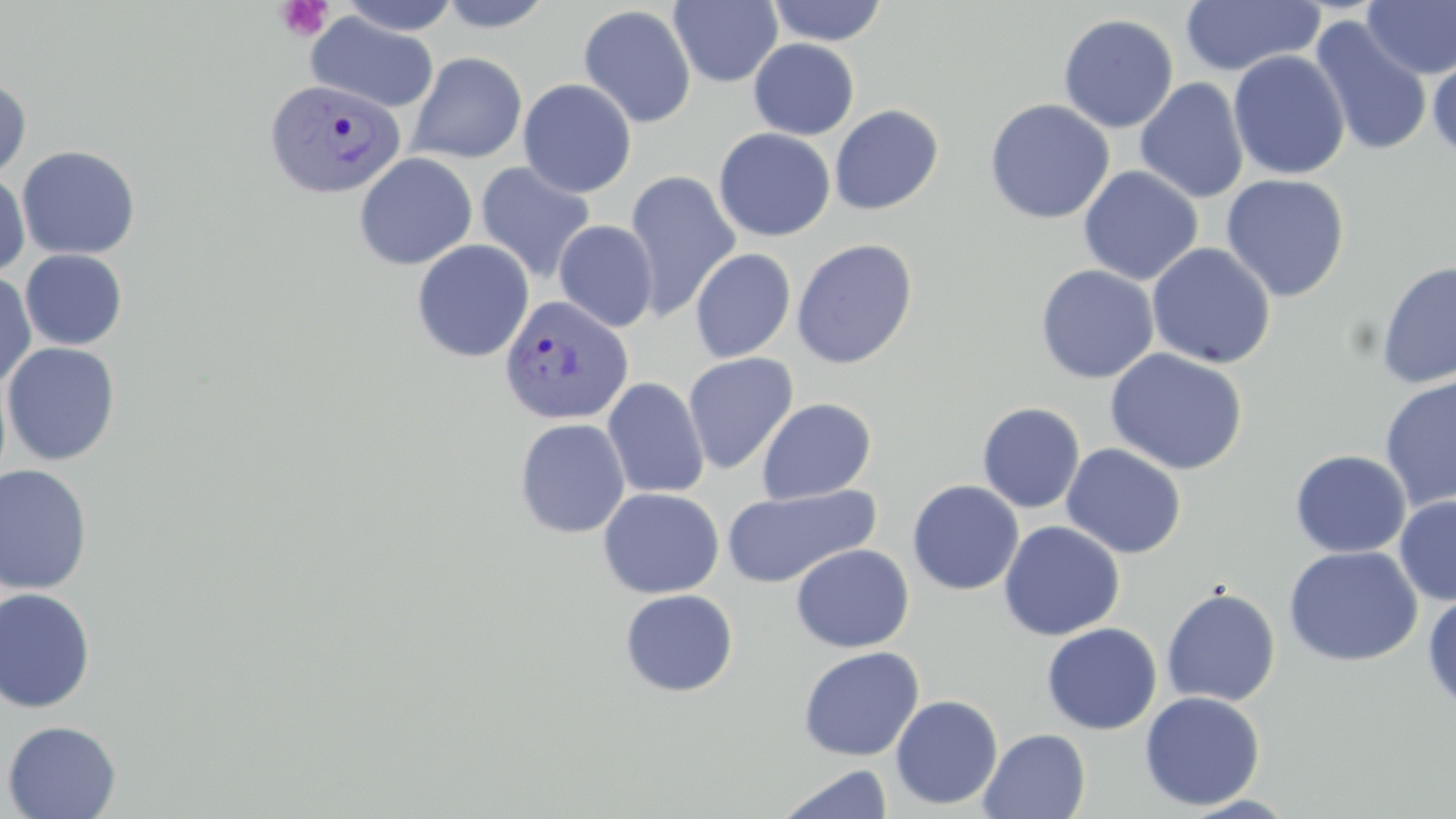

{
  "slide_level_diagnosis": "Plasmodium vivax",
  "image_size": "1456×819 pixels",
  "field_of_view": "single",
  "stain": "May-Grünwald-Giemsa",
  "plasmodium_vivax_infected_red_blood_cell_locations": "approximate bounding boxes as (x1, y1, x2, y2) in pixels: (263, 77, 406, 202), (499, 295, 634, 426)",
  "uninfected_red_blood_cell_locations": "approximate bounding boxes as (x1, y1, x2, y2) in pixels: (437, 0, 555, 32), (668, 0, 783, 87), (1179, 0, 1324, 77), (338, 1, 460, 35), (766, 1, 888, 46), (1361, 1, 1456, 79), (578, 5, 696, 128), (306, 13, 438, 113), (1057, 13, 1179, 133), (1308, 15, 1433, 157), (748, 39, 860, 140), (1428, 47, 1456, 163), (1228, 50, 1350, 181), (407, 52, 527, 164), (0, 77, 31, 182), (1135, 77, 1249, 204), (517, 78, 637, 198), (984, 98, 1115, 224), (829, 104, 944, 215), (713, 128, 836, 242), (17, 145, 141, 260), (354, 152, 478, 271), (475, 161, 597, 284), (1078, 165, 1203, 286), (624, 170, 741, 321), (0, 171, 30, 278), (1220, 173, 1350, 302), (554, 220, 658, 333), (791, 238, 918, 369), (411, 240, 535, 362), (1147, 242, 1276, 369), (19, 249, 128, 350), (690, 249, 796, 363), (1375, 259, 1456, 390), (1035, 264, 1159, 384), (0, 272, 37, 388), (1, 342, 121, 466), (1105, 348, 1248, 475), (682, 353, 799, 474), (1378, 373, 1456, 511), (602, 378, 710, 499), (757, 398, 876, 504), (977, 402, 1085, 513), (514, 418, 631, 538), (1061, 443, 1187, 559), (1290, 450, 1411, 558), (0, 464, 94, 594), (907, 480, 1024, 595), (721, 485, 878, 588), (598, 487, 724, 599), (1394, 496, 1456, 607), (998, 521, 1125, 641), (791, 544, 914, 652), (1283, 546, 1422, 666), (0, 587, 98, 713), (1161, 587, 1281, 707), (619, 589, 738, 697), (1422, 590, 1456, 715), (1041, 622, 1162, 735), (798, 646, 924, 761), (1139, 691, 1265, 811), (889, 694, 1003, 810), (2, 720, 121, 818), (979, 728, 1091, 818), (777, 764, 893, 819)",
  "modality": "optical microscopy",
  "preparation": "thin blood smear",
  "platelet_locations": "approximate bounding boxes as (x1, y1, x2, y2) in pixels: (275, 0, 332, 41)",
  "magnification": "1000x"
}